Identify the cell.
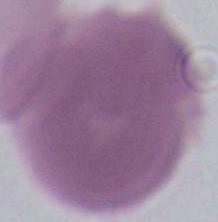
An erythrocyte.

1000x magnification. Photomicrograph.